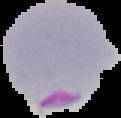
Summary:
  - Image size: 121×118 pixels
  - Malaria status: parasitized
  - Preparation: thin blood smear
  - Image type: cell region segmented out of the field of view; surrounding area masked to black